Locate every blood parasite and identify its species.
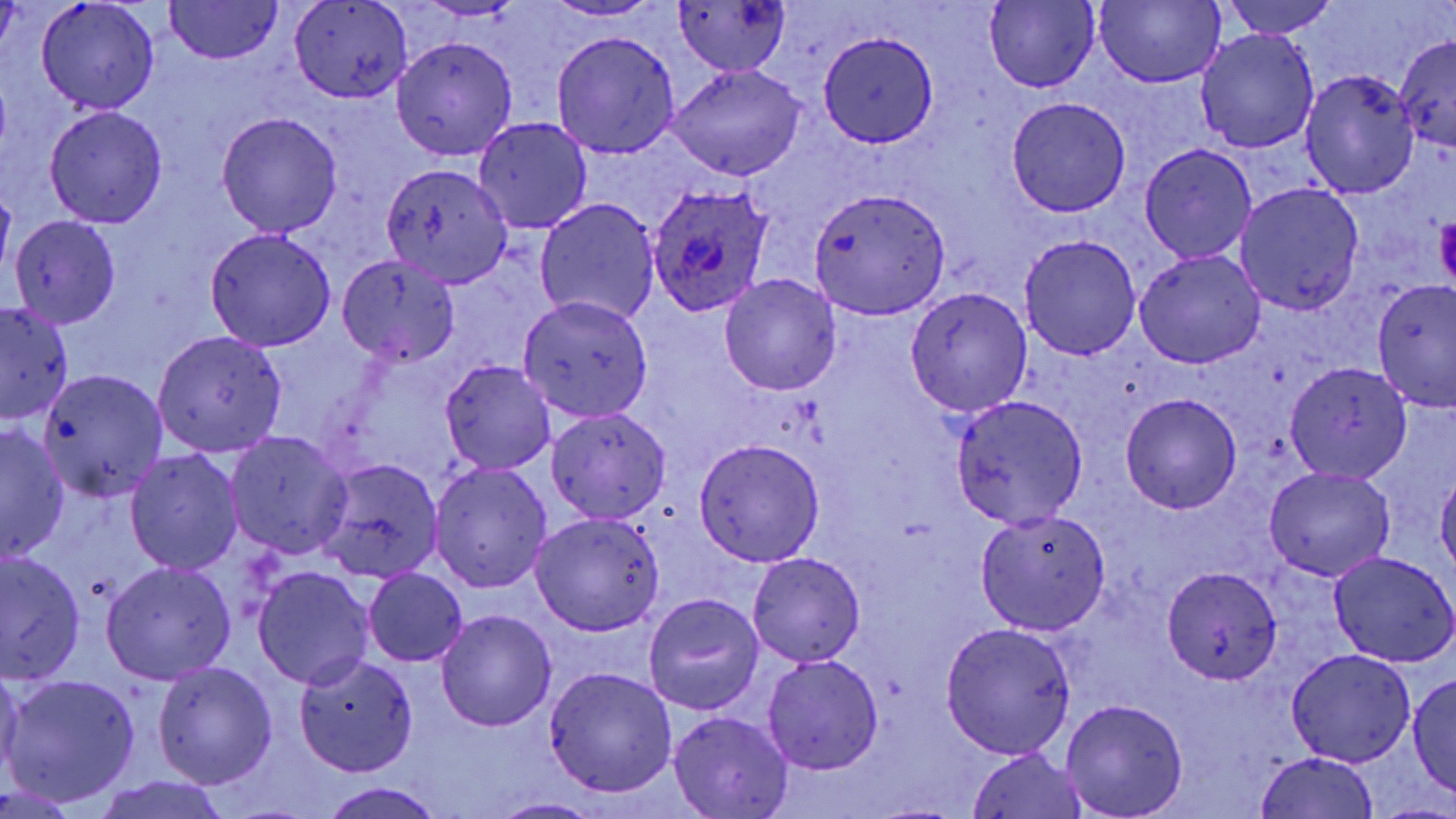

Approximate bounding boxes as named x1/y1/x2/y2 corners in pixels.
Plasmodium ovale-infected red blood cells: (x1=646, y1=182, x2=775, y2=318).
No Plasmodium falciparum, Plasmodium malariae, Plasmodium vivax, Babesia divergens, or Trypanosoma brucei observed.

Uninfected red blood cell locations: (x1=674, y1=0, x2=792, y2=78), (x1=1218, y1=0, x2=1338, y2=39), (x1=37, y1=1, x2=159, y2=114), (x1=165, y1=1, x2=284, y2=64), (x1=546, y1=1, x2=660, y2=20), (x1=290, y1=2, x2=413, y2=103), (x1=984, y1=2, x2=1098, y2=91), (x1=1093, y1=2, x2=1224, y2=88), (x1=1196, y1=27, x2=1321, y2=153), (x1=549, y1=30, x2=679, y2=158), (x1=819, y1=31, x2=937, y2=147), (x1=1394, y1=32, x2=1456, y2=153), (x1=391, y1=35, x2=519, y2=161), (x1=665, y1=63, x2=806, y2=181), (x1=1299, y1=70, x2=1420, y2=198), (x1=1006, y1=98, x2=1131, y2=216), (x1=44, y1=105, x2=168, y2=227), (x1=215, y1=112, x2=344, y2=236), (x1=473, y1=116, x2=593, y2=233), (x1=1140, y1=143, x2=1256, y2=263), (x1=379, y1=163, x2=514, y2=287), (x1=1236, y1=182, x2=1364, y2=315), (x1=810, y1=186, x2=949, y2=319), (x1=534, y1=198, x2=662, y2=326), (x1=10, y1=215, x2=122, y2=328), (x1=204, y1=229, x2=337, y2=351), (x1=1019, y1=234, x2=1142, y2=359), (x1=1135, y1=250, x2=1265, y2=368), (x1=337, y1=252, x2=461, y2=366), (x1=718, y1=272, x2=842, y2=396), (x1=1372, y1=281, x2=1455, y2=414), (x1=905, y1=284, x2=1034, y2=416), (x1=517, y1=295, x2=654, y2=422), (x1=0, y1=301, x2=73, y2=424), (x1=152, y1=331, x2=288, y2=457), (x1=441, y1=360, x2=556, y2=474), (x1=1284, y1=361, x2=1414, y2=484), (x1=36, y1=369, x2=168, y2=501), (x1=1121, y1=393, x2=1242, y2=513), (x1=950, y1=394, x2=1089, y2=528), (x1=546, y1=406, x2=673, y2=524), (x1=1, y1=425, x2=69, y2=561), (x1=225, y1=430, x2=354, y2=558), (x1=693, y1=439, x2=825, y2=566), (x1=125, y1=448, x2=244, y2=576), (x1=316, y1=457, x2=445, y2=582), (x1=428, y1=461, x2=553, y2=592), (x1=1263, y1=467, x2=1395, y2=580), (x1=1435, y1=468, x2=1456, y2=576), (x1=975, y1=510, x2=1111, y2=635), (x1=530, y1=514, x2=664, y2=635), (x1=1329, y1=549, x2=1456, y2=667), (x1=1, y1=552, x2=87, y2=683), (x1=746, y1=552, x2=866, y2=668), (x1=102, y1=561, x2=237, y2=684), (x1=254, y1=566, x2=375, y2=689), (x1=363, y1=567, x2=469, y2=667), (x1=1163, y1=567, x2=1281, y2=682), (x1=643, y1=593, x2=764, y2=715), (x1=437, y1=610, x2=556, y2=732), (x1=941, y1=622, x2=1077, y2=759), (x1=1285, y1=648, x2=1417, y2=767), (x1=762, y1=652, x2=884, y2=775), (x1=293, y1=654, x2=420, y2=775), (x1=152, y1=660, x2=278, y2=789), (x1=0, y1=665, x2=25, y2=783), (x1=543, y1=666, x2=678, y2=798), (x1=1409, y1=671, x2=1456, y2=798), (x1=4, y1=674, x2=139, y2=807), (x1=1061, y1=698, x2=1189, y2=818), (x1=669, y1=709, x2=793, y2=818), (x1=965, y1=747, x2=1089, y2=819), (x1=1252, y1=751, x2=1383, y2=818), (x1=89, y1=776, x2=233, y2=819), (x1=317, y1=781, x2=447, y2=819), (x1=486, y1=797, x2=606, y2=819). Platelet locations: (x1=1432, y1=218, x2=1454, y2=287). Slide-level diagnosis: Plasmodium ovale. Image is 1456×819 pixels. Thin blood film. Optical microscopy. One field of a larger specimen. May-Grünwald-Giemsa-stained preparation. Captured at 1000x magnification.